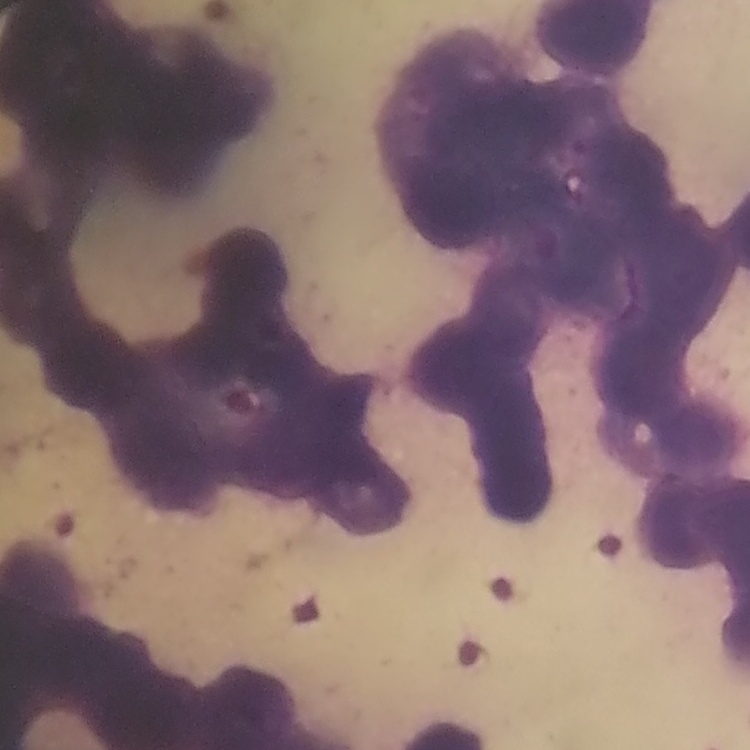
red_blood_cell_morphology: rouleaux formation
preparation: thin blood film
stain: Field's or Giemsa
image_type: one tile cut from a larger photomicrograph